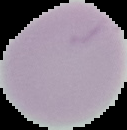

Summary:
  - Preparation: thin blood smear
  - Image type: cell region segmented out of the field of view; surrounding area masked to black
  - Result: no Plasmodium parasites seen
  - Image size: 127×130 pixels